Classify this cell by malaria status.
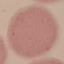
Uninfected.

capture = smartphone through the microscope eyepiece
image type = cell patch, automatically extracted from a larger field of view and resized to 64 × 64 pixels
preparation = thin blood smear
stain = Giemsa